Assess this cell for malaria.
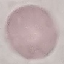
It is uninfected.

{
  "capture": "smartphone through the microscope eyepiece",
  "preparation": "thin blood film",
  "image_type": "cell patch, automatically extracted from a larger field of view and resized to 64 × 64 pixels",
  "stain": "Giemsa"
}